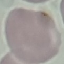 Result: no malaria parasites detected. Photographed with a smartphone camera at the microscope eyepiece. Automatically extracted cell patch, resized to 64 × 64 pixels. Thin blood smear. Giemsa-stained preparation.